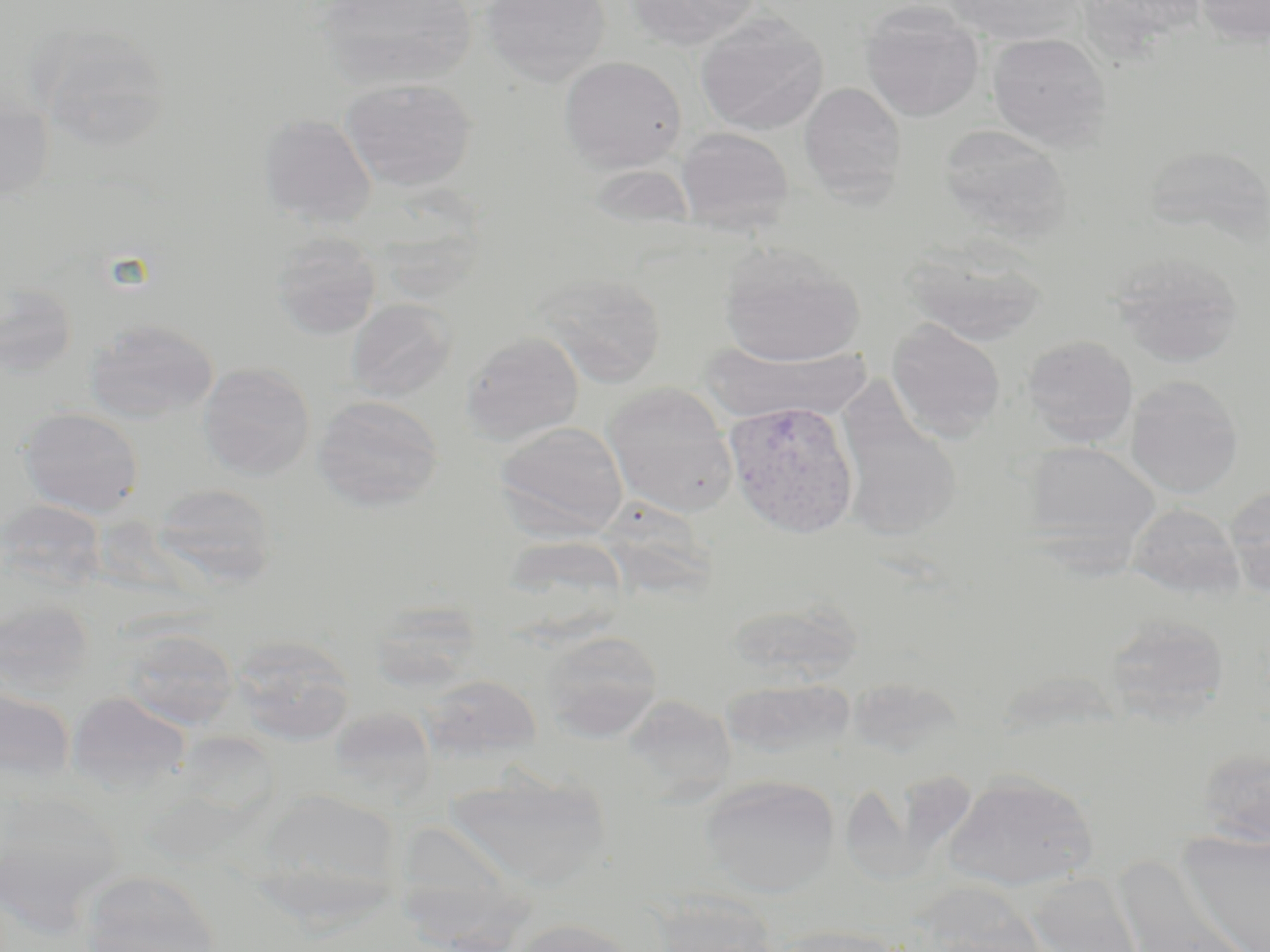 Approximate bounding boxes as (x1,y1)-(x2,y2) corner pairs in pixels. Plasmodium vivax-infected red blood cell locations: (723,399)-(860,539). Uninfected red blood cell locations: (314,0)-(478,90), (479,0)-(612,84), (625,0)-(761,51), (946,0)-(1084,45), (1194,0)-(1270,46), (859,2)-(985,122), (695,13)-(829,135), (32,22)-(173,153), (986,32)-(1112,151), (559,56)-(687,172), (340,77)-(477,191), (798,81)-(907,201), (0,86)-(55,201), (258,114)-(377,228), (938,124)-(1073,241), (675,126)-(794,233), (1144,145)-(1270,246), (270,233)-(382,340), (900,237)-(1048,345), (718,244)-(865,367), (1109,251)-(1245,368), (534,271)-(667,387), (0,280)-(79,379), (346,299)-(456,401), (85,318)-(218,423), (886,319)-(1006,442), (461,330)-(584,445), (1022,334)-(1139,446), (701,342)-(873,426), (197,362)-(315,479), (1125,375)-(1244,498), (602,382)-(739,518), (834,382)-(963,541), (312,394)-(443,512), (18,406)-(145,518), (493,421)-(629,540), (1022,441)-(1162,563), (151,483)-(277,589), (1225,486)-(1270,596), (0,499)-(108,594), (1126,502)-(1244,599), (0,595)-(95,702), (725,599)-(863,688), (368,600)-(486,695), (1103,613)-(1232,723), (116,626)-(239,730), (542,630)-(663,742), (229,634)-(357,745), (423,673)-(542,761), (722,677)-(854,759), (0,684)-(77,790), (66,691)-(192,795), (620,696)-(735,806), (338,708)-(441,811), (1196,746)-(1270,847), (445,768)-(611,890), (942,770)-(1097,891), (848,771)-(979,887), (700,775)-(840,897), (0,788)-(121,935), (252,789)-(405,923), (1176,830)-(1270,952), (1117,857)-(1257,952), (76,872)-(221,952), (1025,873)-(1147,952), (648,892)-(783,952), (507,918)-(641,952), (769,924)-(907,952). Slide-level diagnosis: Plasmodium vivax. Captured at 1000x magnification. May-Grünwald-Giemsa-stained preparation. Image is 1270×952 pixels. Light microscopy. Thin blood smear. Single field of view.